Describe the morphology of the erythrocytes.
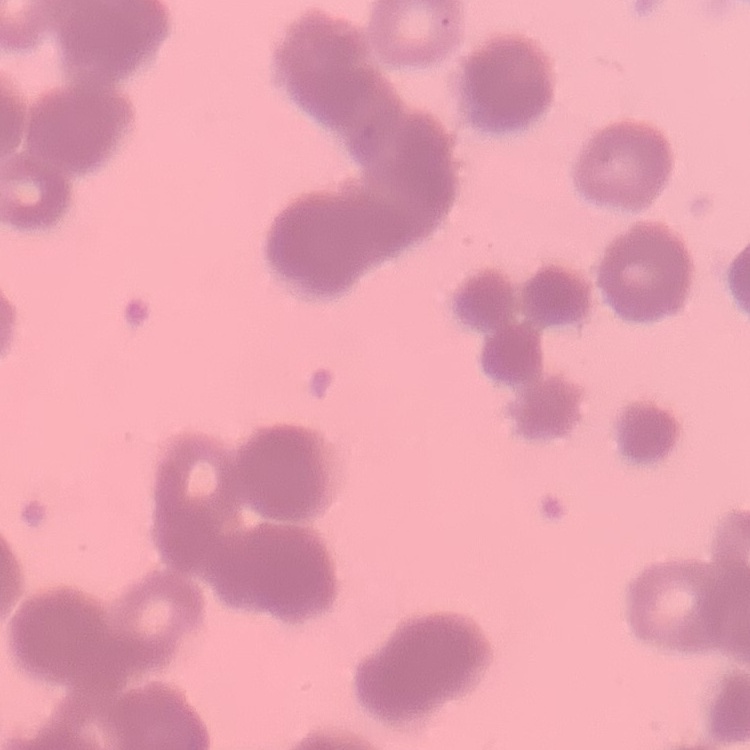
They show rouleaux formation.

stain = Field's or Giemsa
preparation = thin peripheral smear
image type = one tile cut from a larger photomicrograph